Assess this cell for malaria.
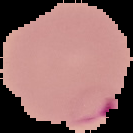

It is parasitized.

image size = 133×133 pixels
image type = segmented cell region on a black background
preparation = thin blood smear